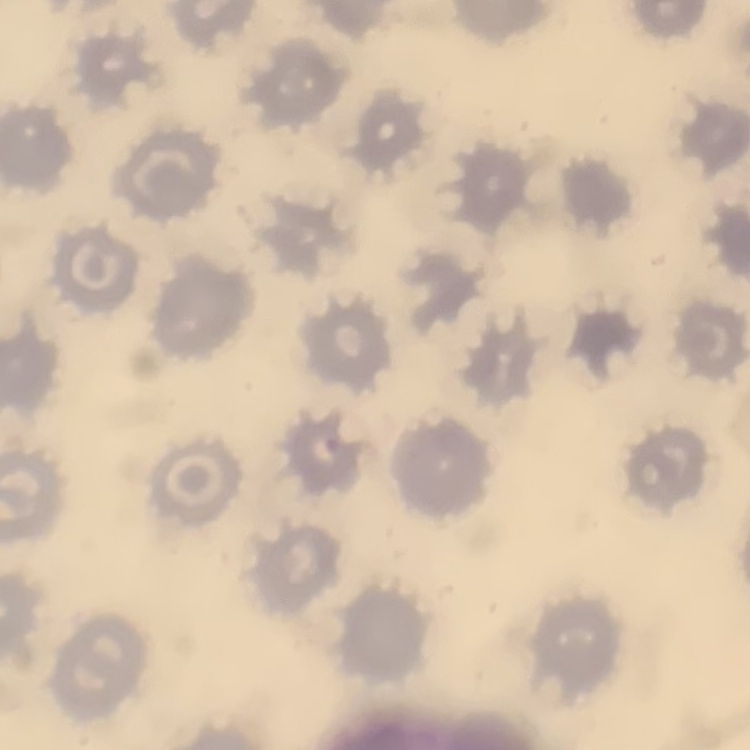 The red blood cells exhibit no rouleaux formation. Field's or Giemsa stain. Square crop of a larger photomicrograph. Thin blood film.